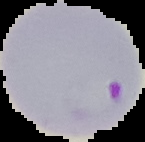

preparation = thin blood smear
malaria status = parasitized
image size = 145×142 pixels
image type = segmented cell region on a black background